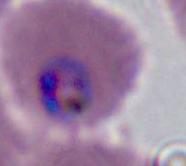
modality = micrograph
identification = Plasmodium
magnification = 400x or 1000x